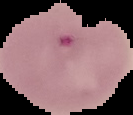

Summary:
  - Preparation: thin blood film
  - Image type: segmented cell region on a black background
  - Image size: 133×115 pixels
  - Result: malaria parasites identified